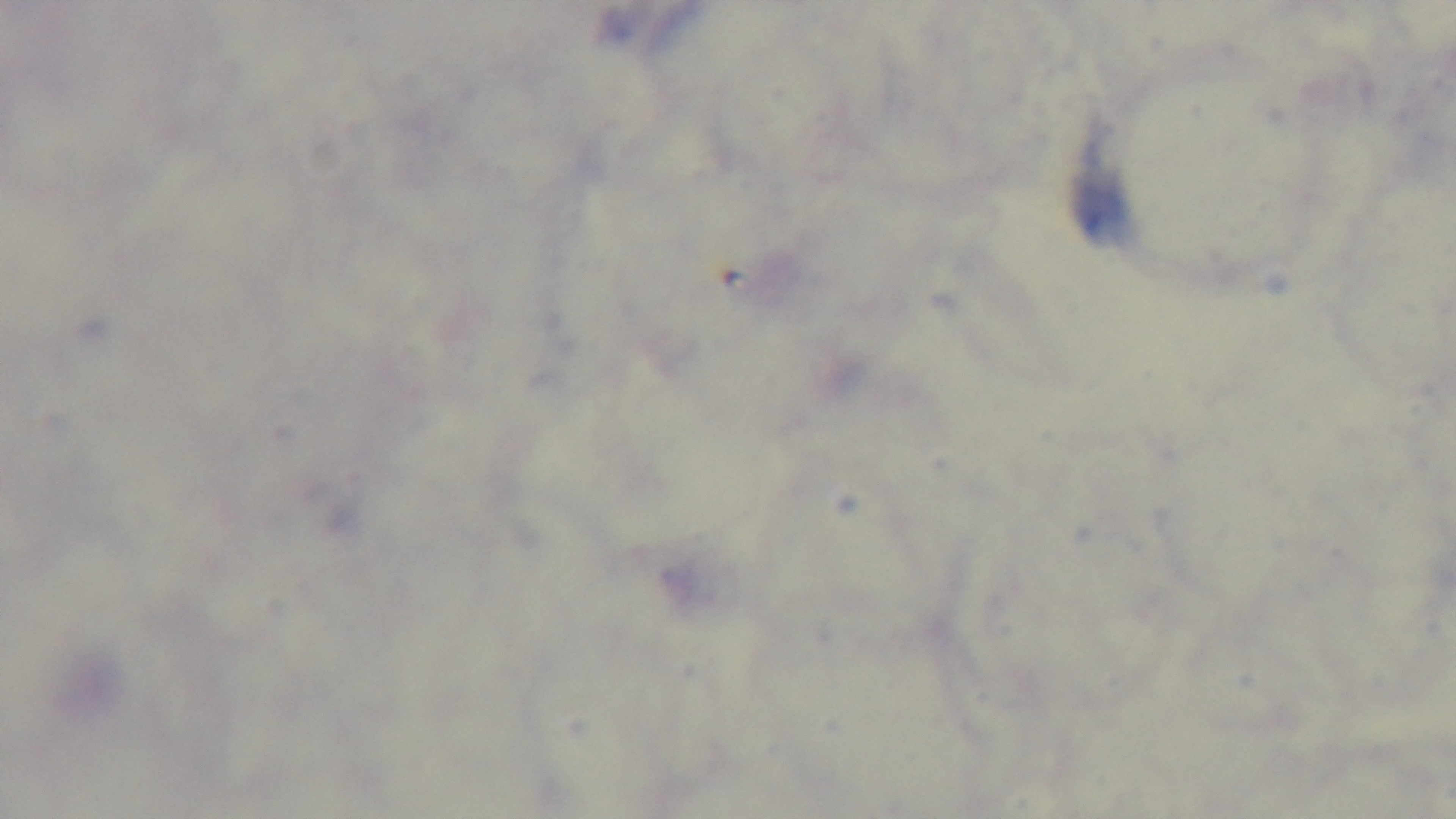
Preparation: thick smear. Giemsa stain. Photomicrograph. 100x oil-immersion objective. Captured with a mounted 4K digital camera. Malaria status: negative. One field from the slide.